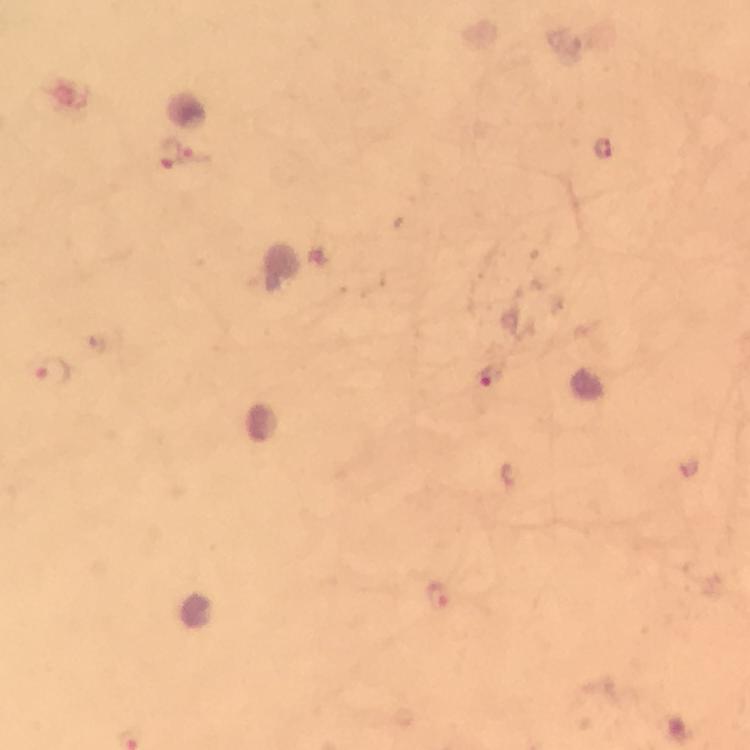

Approximate centers as (x, y) in pixels.
Summary:
  - Malaria parasite locations: (602, 150), (170, 152), (196, 156), (53, 371), (490, 377), (440, 598)
  - Stain: Giemsa
  - Image size: 750×750 pixels
  - Capture: smartphone mounted on the microscope
  - Cropped from: one field of view
  - Preparation: thick blood smear
  - Immersion oil: applied
  - Context: from a diagnostic examination for malaria
  - Magnification: 100x